Assess this cell for malaria.
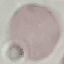
It is uninfected.

{
  "image_type": "automatically extracted cell patch, resized to 64 × 64 pixels",
  "preparation": "thin blood smear",
  "stain": "Giemsa",
  "capture": "smartphone camera at the microscope eyepiece"
}